Identify the blood parasite species.
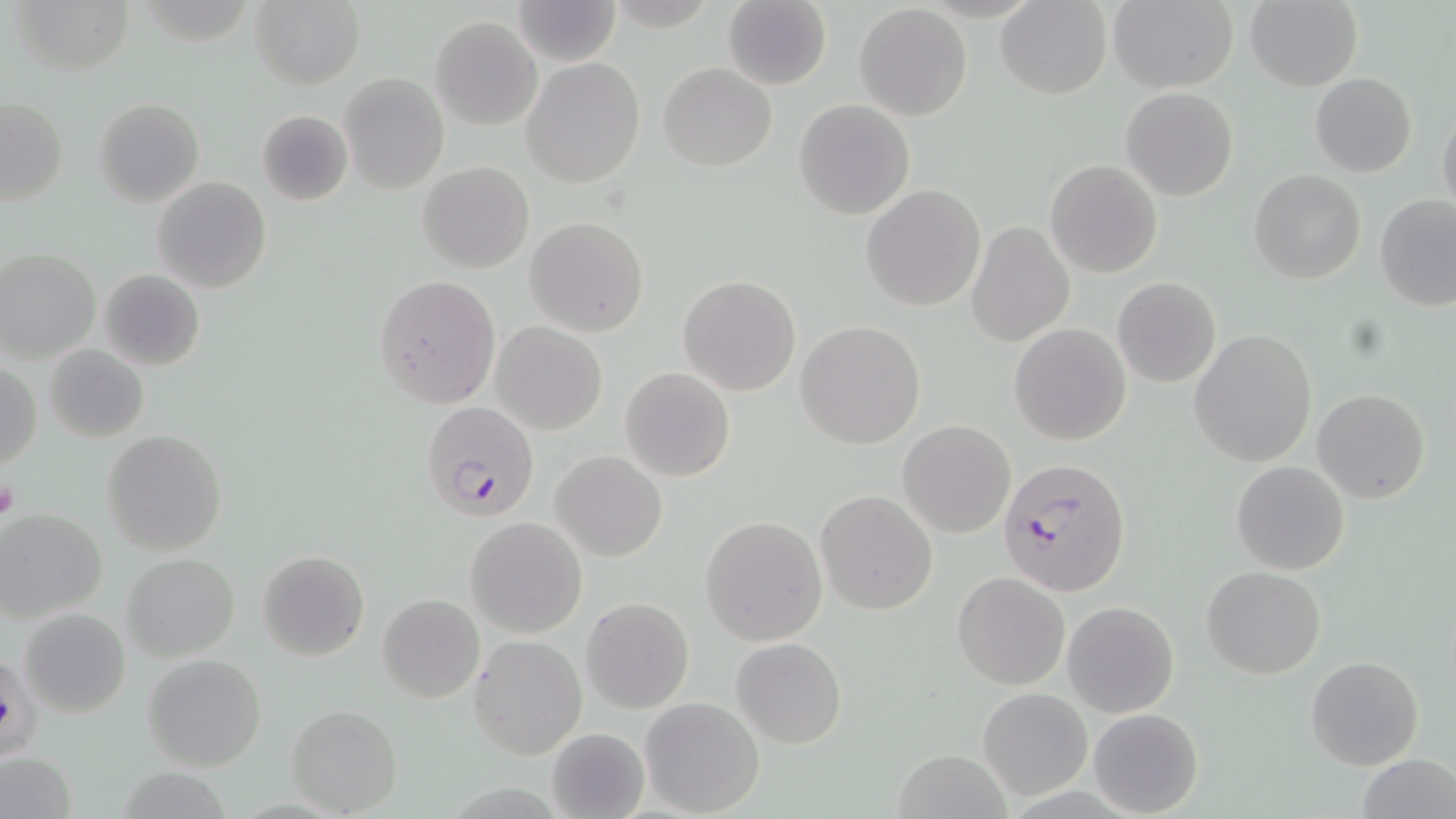
Plasmodium falciparum.

stain = May-Grünwald-Giemsa
field of view = single
modality = optical microscopy
Plasmodium falciparum-infected red blood cell locations = approximate bounding boxes as named x1/y1/x2/y2 corners in pixels: (x1=421, y1=401, x2=541, y2=521), (x1=998, y1=457, x2=1132, y2=597)
platelet locations = approximate bounding boxes as named x1/y1/x2/y2 corners in pixels: (x1=0, y1=476, x2=20, y2=523)
magnification = 1000x
preparation = thin blood smear
image size = 1456×819 pixels
uninfected red blood cell locations = approximate bounding boxes as named x1/y1/x2/y2 corners in pixels: (x1=9, y1=0, x2=134, y2=74), (x1=513, y1=0, x2=621, y2=66), (x1=995, y1=0, x2=1111, y2=100), (x1=1108, y1=0, x2=1241, y2=93), (x1=1245, y1=0, x2=1363, y2=92), (x1=249, y1=1, x2=365, y2=88), (x1=721, y1=1, x2=832, y2=90), (x1=854, y1=4, x2=973, y2=121), (x1=431, y1=15, x2=542, y2=130), (x1=520, y1=56, x2=645, y2=188), (x1=659, y1=63, x2=776, y2=171), (x1=1310, y1=72, x2=1416, y2=177), (x1=339, y1=73, x2=448, y2=194), (x1=1121, y1=87, x2=1238, y2=202), (x1=0, y1=96, x2=68, y2=204), (x1=94, y1=97, x2=204, y2=206), (x1=793, y1=99, x2=914, y2=220), (x1=1437, y1=107, x2=1456, y2=219), (x1=256, y1=110, x2=353, y2=205), (x1=1046, y1=159, x2=1162, y2=278), (x1=417, y1=161, x2=534, y2=275), (x1=1248, y1=169, x2=1365, y2=284), (x1=153, y1=176, x2=271, y2=293), (x1=861, y1=185, x2=986, y2=312), (x1=1372, y1=193, x2=1456, y2=311), (x1=525, y1=217, x2=649, y2=338), (x1=965, y1=220, x2=1076, y2=347), (x1=0, y1=248, x2=100, y2=363), (x1=97, y1=269, x2=206, y2=372), (x1=677, y1=274, x2=802, y2=396), (x1=375, y1=276, x2=500, y2=407), (x1=1112, y1=277, x2=1222, y2=388), (x1=796, y1=320, x2=925, y2=449), (x1=490, y1=321, x2=607, y2=435), (x1=1009, y1=322, x2=1131, y2=445), (x1=1189, y1=329, x2=1316, y2=467), (x1=43, y1=343, x2=148, y2=443), (x1=1, y1=364, x2=41, y2=470), (x1=620, y1=367, x2=735, y2=481), (x1=1313, y1=389, x2=1431, y2=504), (x1=897, y1=420, x2=1016, y2=538), (x1=102, y1=429, x2=228, y2=556), (x1=551, y1=450, x2=667, y2=562), (x1=1231, y1=461, x2=1349, y2=574), (x1=815, y1=490, x2=938, y2=615), (x1=1, y1=509, x2=108, y2=622), (x1=700, y1=515, x2=827, y2=647), (x1=465, y1=517, x2=586, y2=639), (x1=257, y1=549, x2=369, y2=662), (x1=121, y1=552, x2=240, y2=661), (x1=1201, y1=565, x2=1326, y2=679), (x1=952, y1=572, x2=1071, y2=691), (x1=377, y1=593, x2=485, y2=704), (x1=580, y1=597, x2=695, y2=714), (x1=1062, y1=602, x2=1179, y2=718), (x1=20, y1=608, x2=131, y2=717), (x1=468, y1=636, x2=587, y2=760), (x1=732, y1=637, x2=846, y2=749), (x1=144, y1=655, x2=266, y2=770), (x1=1305, y1=656, x2=1426, y2=771), (x1=976, y1=686, x2=1094, y2=800), (x1=639, y1=697, x2=766, y2=818), (x1=286, y1=705, x2=402, y2=816), (x1=1088, y1=707, x2=1204, y2=817), (x1=546, y1=727, x2=650, y2=819), (x1=895, y1=748, x2=1012, y2=819), (x1=0, y1=751, x2=77, y2=819), (x1=1355, y1=756, x2=1456, y2=819)